Point out each malaria parasite.
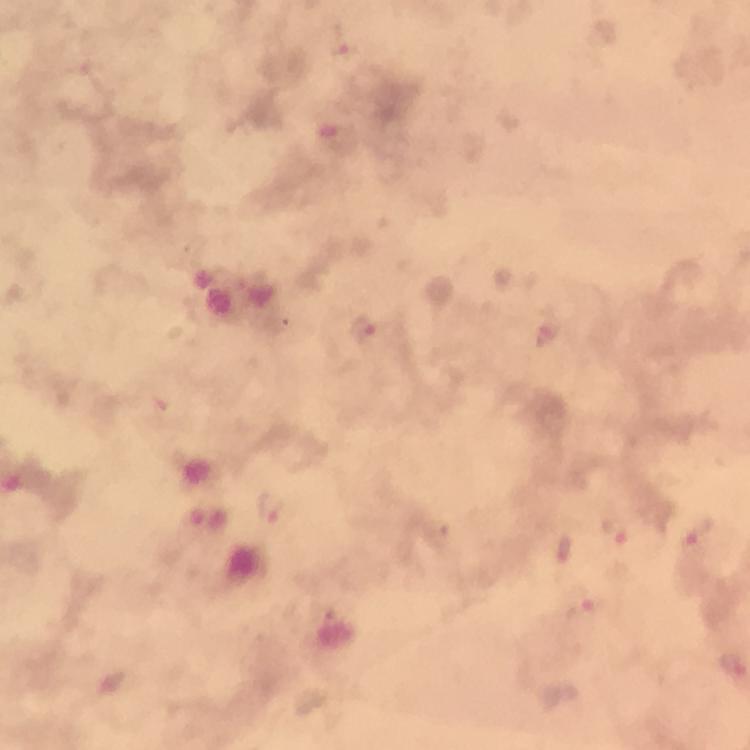

Approximate object centers, in pixels from the top-left corner.
Malaria parasites: (x=340, y=40), (x=548, y=329), (x=362, y=330), (x=269, y=507), (x=615, y=533), (x=698, y=533), (x=565, y=551), (x=578, y=609).

Cropped region of a single field of view. At 100x magnification. Thick smear. Immersion oil applied. Giemsa stain. Image is 750×750 pixels. Smartphone photograph taken through a microscope. From a diagnostic examination for malaria.